Report the malaria status of this cell.
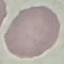

It is uninfected.

Giemsa-stained preparation. Cell patch, automatically extracted from a larger field of view and resized to 64 × 64 pixels. Acquired by smartphone through the microscope eyepiece. Thin blood smear.